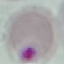

Result: no malaria parasites seen. Giemsa stain. Automatically extracted cell patch, resized to 64 × 64 pixels. Acquired by smartphone through the microscope eyepiece. Thin smear of blood.